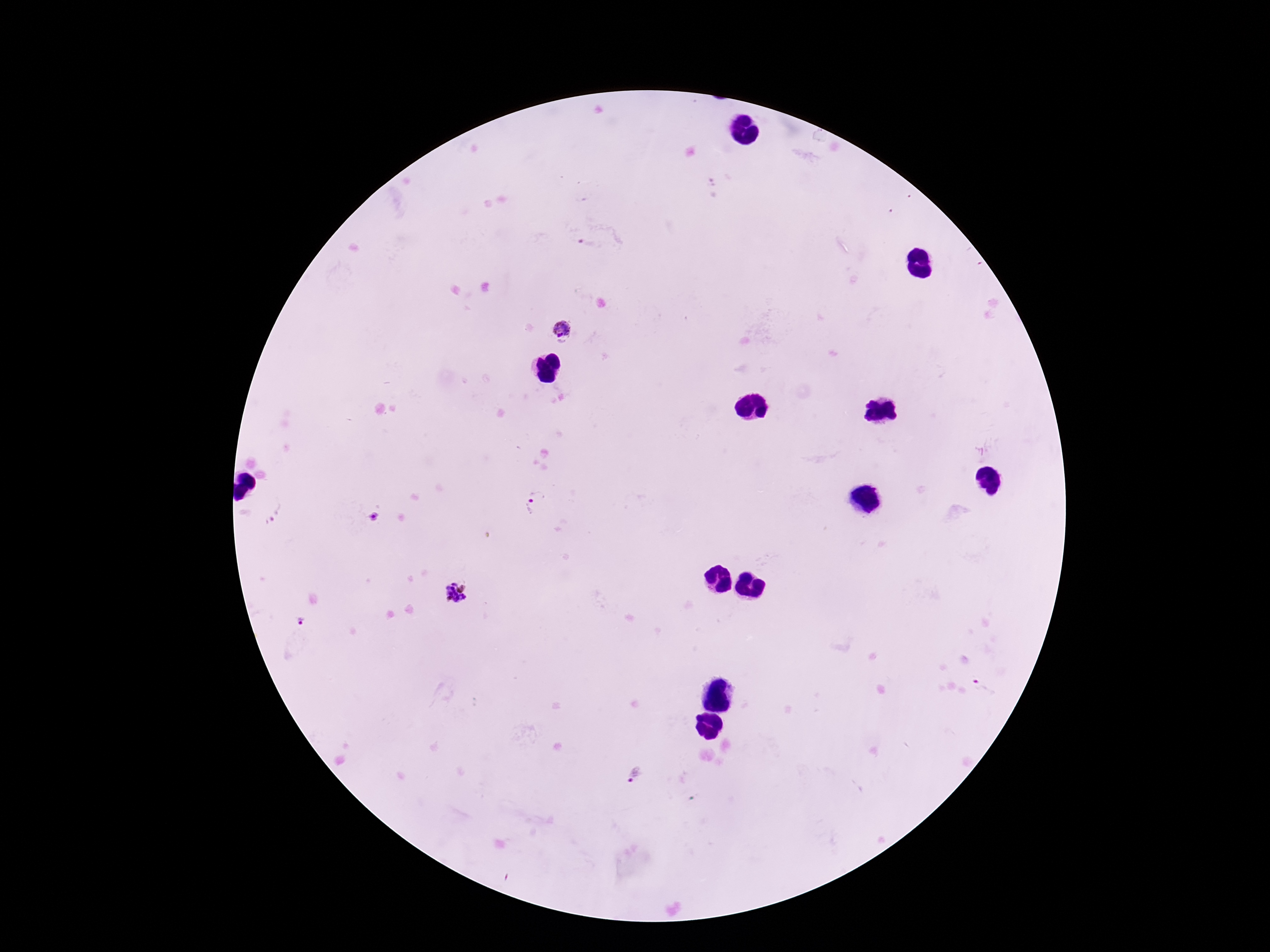
Approximate centers as [x, y] in pixels. Plasmodium parasite locations: [587, 245], [562, 329], [534, 503], [457, 593], [984, 687], [636, 774]. Thick peripheral-blood smear. Smartphone photograph taken through the microscope eyepiece. Giemsa-stained preparation. Image is 1270×952 pixels. 100x magnification. Patient malaria status: infected. One field from this slide.